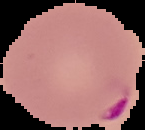

Summary:
  - Malaria status: parasitized
  - Image type: segmented cell region on a black background
  - Image size: 145×130 pixels
  - Preparation: thin blood film